Report the malaria status of this cell.
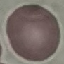
Uninfected.

Summary:
  - Capture: smartphone camera at the microscope eyepiece
  - Preparation: thin blood film
  - Stain: Giemsa
  - Image type: automatically extracted cell patch, resized to 64 × 64 pixels